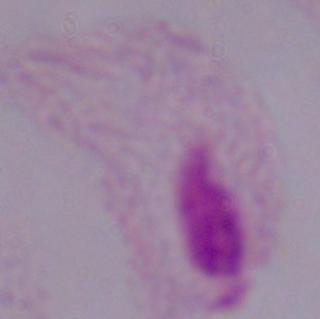
magnification = 1000x
modality = photomicrograph
identification = trichomonad